Assess for Plasmodium parasites.
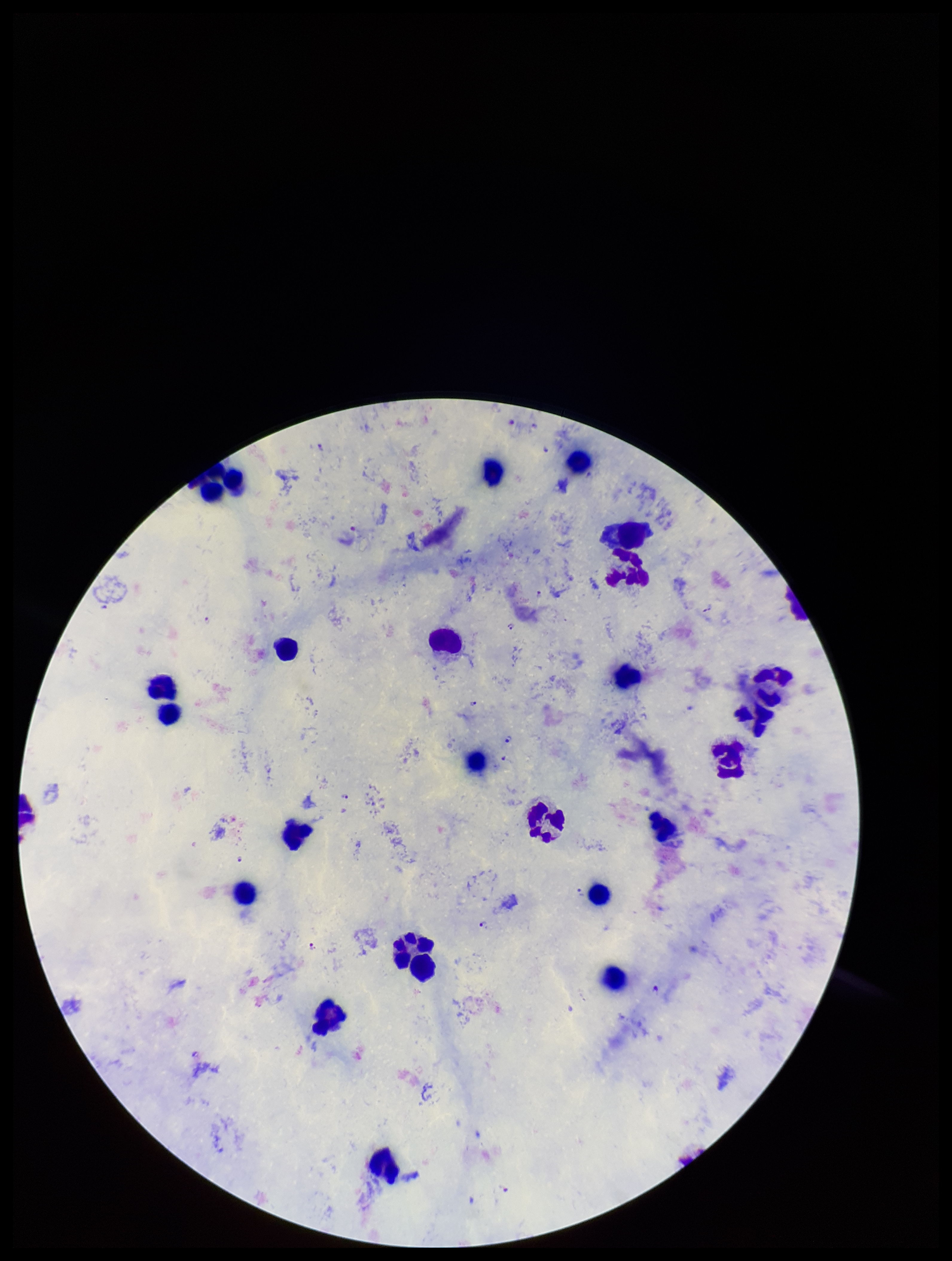
Identified.

Parasite count: 12. Smartphone photograph taken through the eyepiece of a microscope. Leukocyte count: 22. Preparation: thick. One field from this slide. Patient malaria status: positive. Image is 952×1261 pixels. Species reported for this patient: Plasmodium falciparum. Stained with Giemsa.